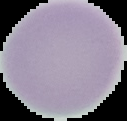

Summary:
  - Preparation: thin blood film
  - Image type: cell region segmented out of the field of view; surrounding area masked to black
  - Result: no Plasmodium parasites seen
  - Image size: 127×121 pixels